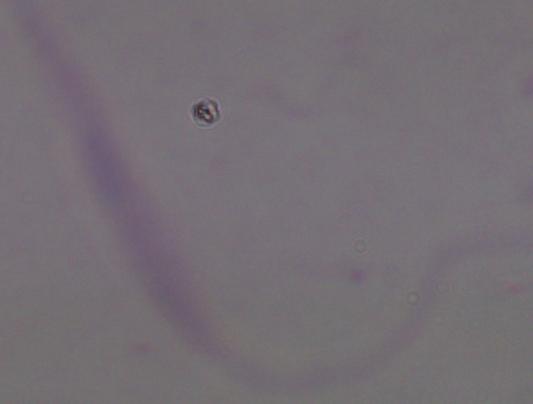

Summary:
  - Identification: Leishmania
  - Magnification: 1000x
  - Modality: photomicrograph